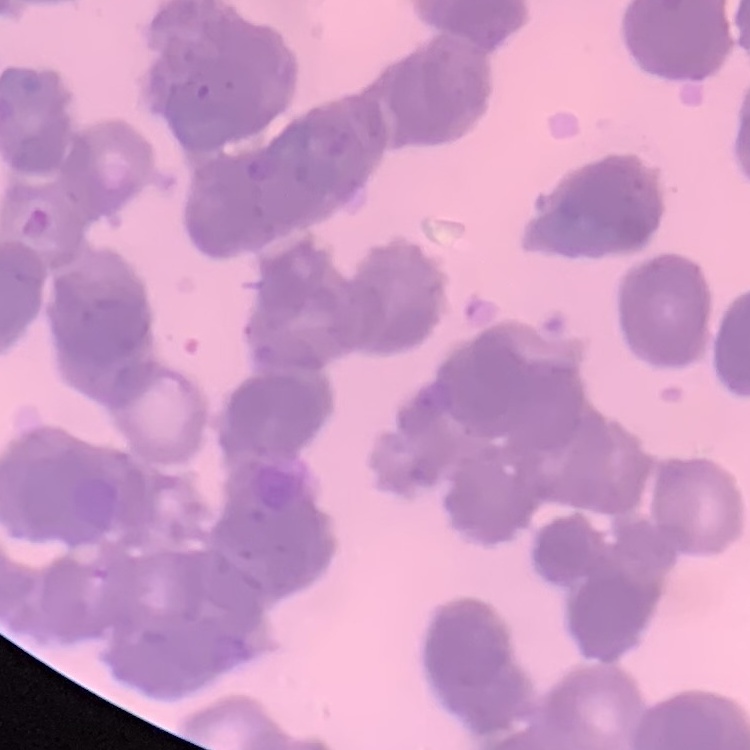
{
  "erythrocyte_morphology": "rouleaux formation",
  "stain": "Field's or Giemsa",
  "image_type": "one tile cut from a larger photomicrograph",
  "preparation": "thin blood smear"
}